Comment on the morphology of the red blood cells.
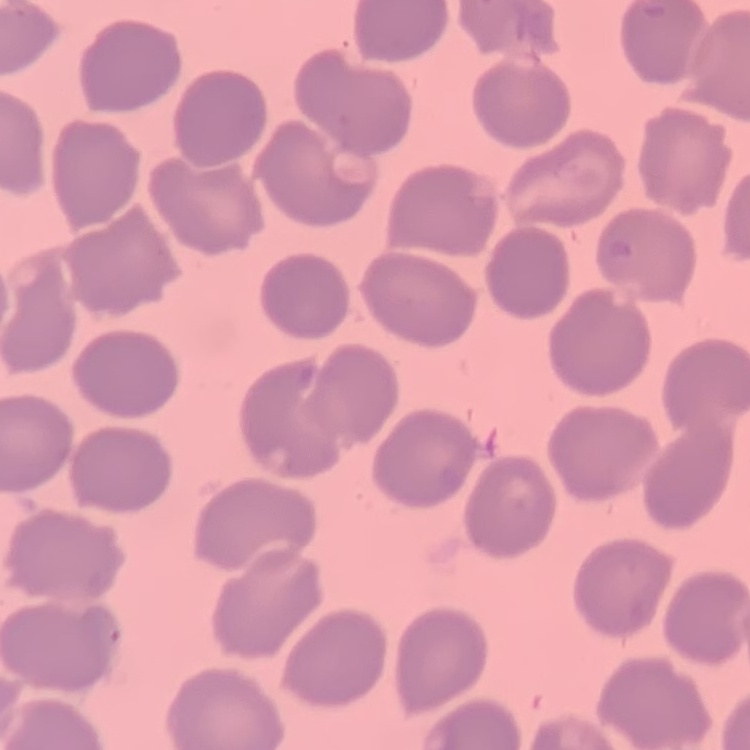
They show no rouleaux formation.

Stained with either Field's or Giemsa. Thin blood smear. Square crop of a larger photomicrograph.